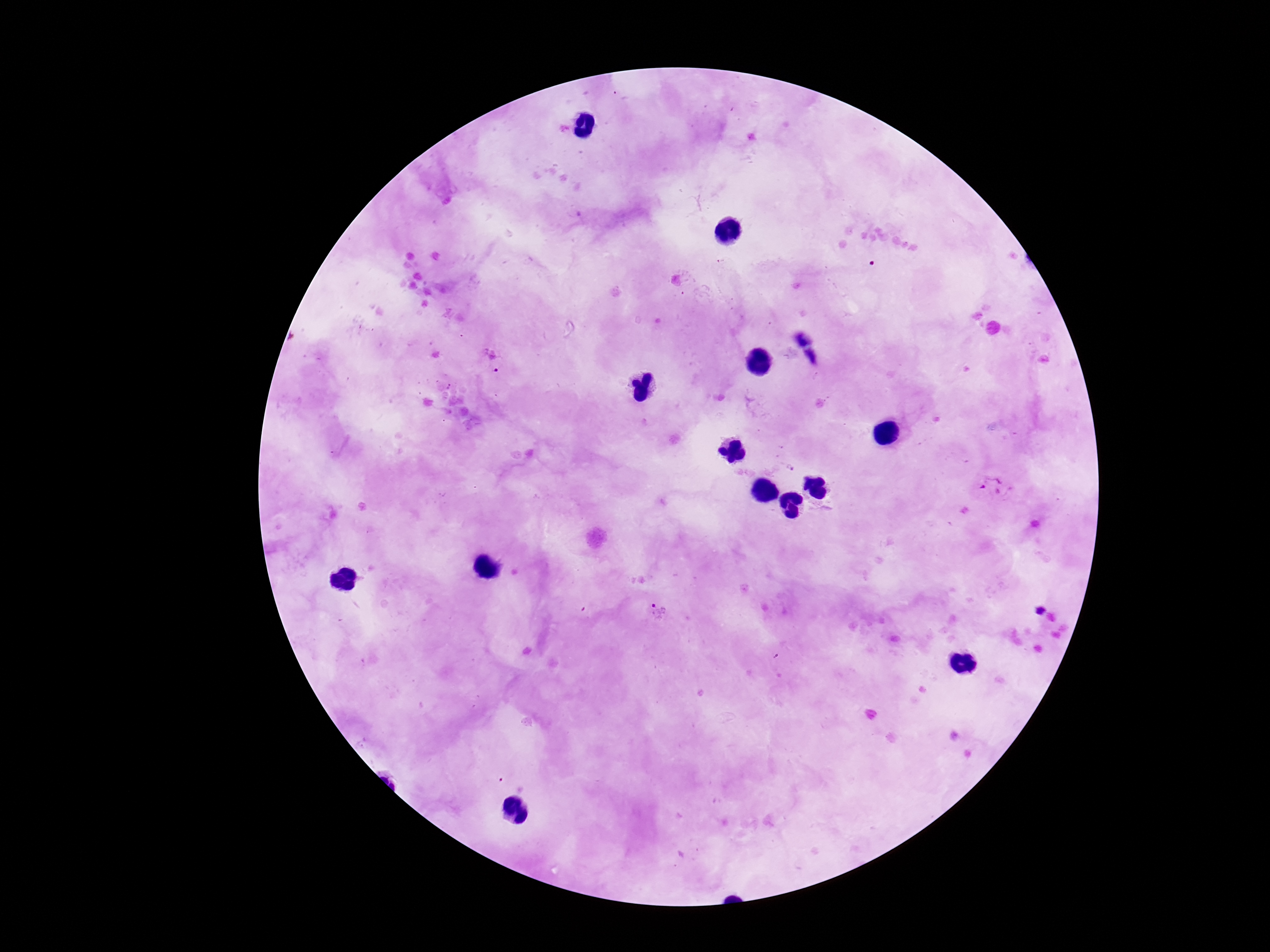 Approximate centers as {x, y} in pixels. Plasmodium parasite locations: {495, 364}, {991, 491}, {661, 613}. Thick blood smear. Giemsa-stained preparation. 100x magnification. Image is 1270×952 pixels. Patient malaria status: infected. Single field of view. Smartphone photograph taken through the microscope eyepiece.